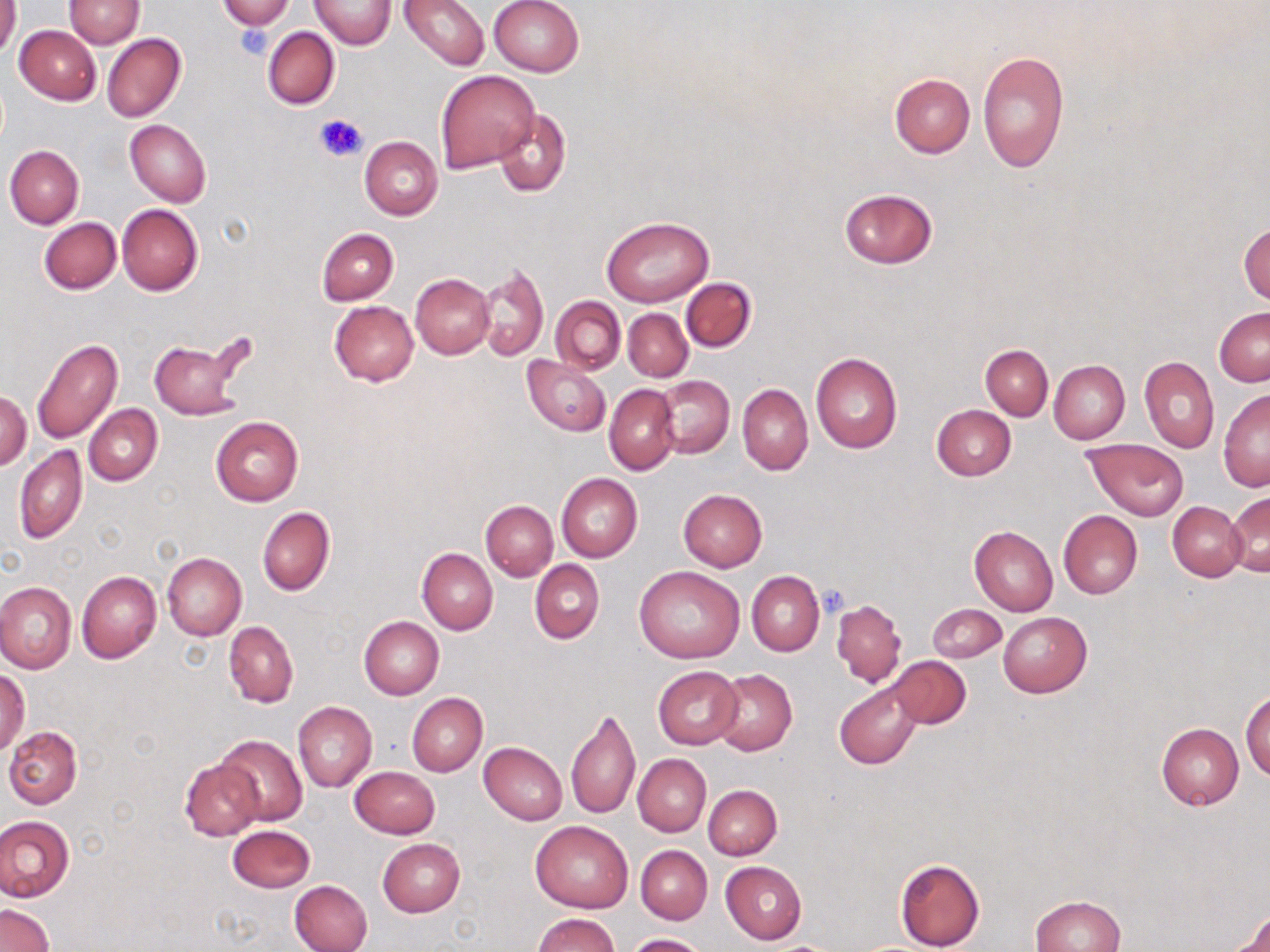 Approximate bounding boxes as [x1, y1, x2, y2] in pixels. Platelet locations: [236, 24, 275, 60], [315, 113, 370, 162], [819, 586, 848, 619]. Uninfected red blood cell locations: [0, 0, 20, 60], [64, 0, 143, 48], [217, 0, 295, 30], [309, 0, 397, 48], [400, 0, 488, 70], [489, 0, 584, 77], [14, 25, 101, 105], [262, 27, 339, 110], [102, 33, 186, 122], [976, 50, 1069, 174], [435, 69, 539, 172], [889, 74, 975, 158], [493, 108, 571, 198], [124, 119, 211, 208], [360, 137, 442, 220], [4, 145, 84, 228], [839, 188, 938, 268], [118, 205, 203, 295], [601, 215, 713, 307], [39, 217, 121, 293], [1239, 222, 1269, 305], [317, 227, 398, 305], [476, 262, 548, 361], [410, 273, 494, 358], [681, 278, 756, 351], [550, 296, 624, 374], [329, 300, 419, 386], [1215, 307, 1270, 386], [623, 309, 692, 381], [147, 337, 246, 420], [31, 338, 123, 444], [981, 345, 1052, 419], [811, 353, 902, 453], [522, 356, 610, 437], [1140, 356, 1219, 452], [1049, 360, 1129, 444], [654, 375, 734, 459], [604, 384, 679, 474], [737, 384, 812, 475], [0, 390, 31, 471], [1218, 390, 1269, 491], [84, 404, 162, 486], [931, 404, 1016, 481], [210, 416, 303, 506], [1083, 438, 1189, 520], [14, 446, 88, 543], [556, 474, 642, 563], [678, 488, 766, 571], [1227, 493, 1270, 576], [481, 499, 558, 581], [1168, 502, 1247, 581], [257, 506, 336, 596], [1057, 510, 1141, 598], [968, 526, 1058, 615], [417, 548, 496, 634], [161, 553, 246, 640], [529, 559, 604, 644], [635, 566, 745, 663], [76, 570, 161, 664], [747, 570, 824, 656], [0, 582, 76, 674], [831, 600, 906, 686], [927, 603, 1006, 662], [998, 612, 1091, 697], [360, 616, 443, 699], [224, 620, 298, 708], [889, 656, 971, 728], [652, 666, 743, 749], [0, 670, 30, 754], [712, 670, 797, 756], [834, 682, 924, 770], [1241, 689, 1269, 781], [407, 692, 487, 777], [293, 701, 377, 792], [567, 706, 641, 820], [1157, 723, 1245, 809], [4, 726, 82, 808], [216, 734, 307, 826], [479, 742, 568, 824], [633, 754, 710, 837], [180, 757, 264, 841], [349, 767, 440, 839], [704, 784, 781, 860], [0, 815, 74, 903], [530, 820, 634, 913], [228, 824, 315, 892], [377, 838, 465, 917], [636, 845, 711, 923], [895, 858, 985, 951], [720, 861, 807, 943], [289, 879, 373, 952], [1030, 896, 1123, 952], [0, 905, 53, 952], [1228, 911, 1270, 952], [532, 914, 620, 952], [628, 933, 709, 952]. Slide-level diagnosis: negative for blood parasites. May-Grünwald-Giemsa stain. Captured at 1000x magnification. Thin blood smear. Image is 1270×952 pixels. One field of a larger specimen. Light microscopy.